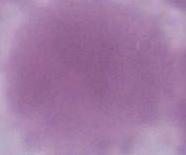 An erythrocyte is shown. Photomicrograph. Captured at 1000x magnification.